Report the malaria status of this cell.
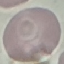

It is uninfected.

stain = Giemsa
preparation = thin blood smear
image type = automatically extracted cell patch, resized to 64 × 64 pixels
capture = smartphone camera at the microscope eyepiece